Give the position of every leukocyte visible.
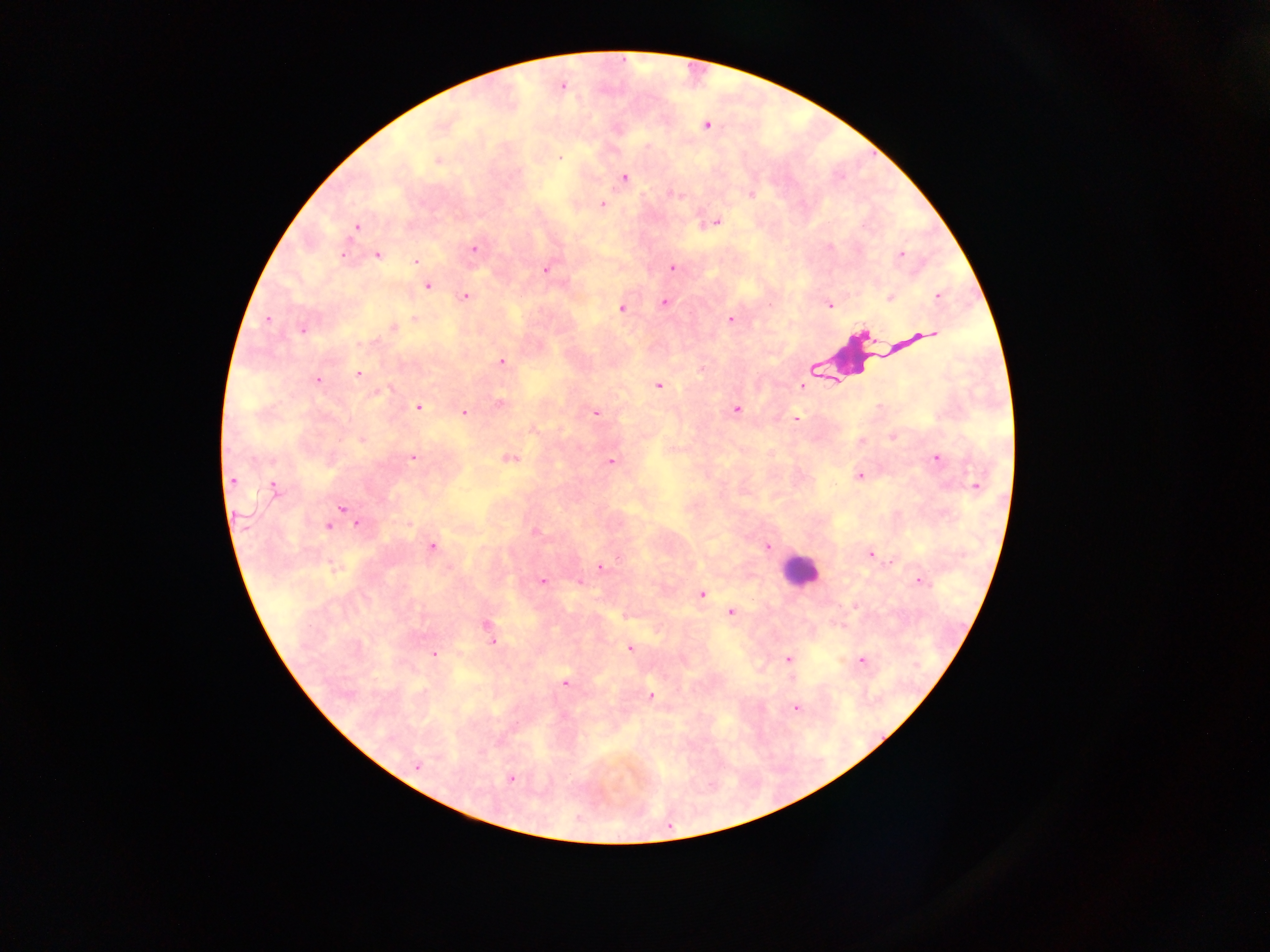
Approximate centers as x y in pixels.
Leukocytes: 858 358; 799 570.

Summary:
  - Plasmodium parasite locations: 707 126; 559 158; 438 160; 624 177; 602 204; 716 222; 356 227; 830 246; 473 248; 343 254; 901 254; 378 255; 415 261; 673 267; 546 270; 427 286; 466 296; 938 296; 890 298; 665 303; 829 305; 621 308; 414 319; 730 319; 267 320; 393 327; 302 330; 930 334; 502 362; 358 373; 317 380; 658 385; 801 386; 389 390; 499 404; 879 406; 418 407; 736 410; 464 412; 596 413; 795 419; 892 437; 360 441; 413 457; 936 458; 509 459; 611 461; 858 476; 232 480; 975 485; 274 488; 342 507; 358 524; 408 525; 328 526; 535 532; 432 546; 767 547; 870 555; 601 567; 542 580; 919 581; 580 583; 702 594; 731 612; 486 624; 492 642; 630 648; 433 655; 787 659; 862 660; 565 683; 651 696; 796 707; 416 766; 511 778
  - Capture: mobile-phone photograph through a microscope
  - Field of view: single
  - Preparation: thick blood smear
  - Country: Ghana
  - Image size: 1270×952 pixels